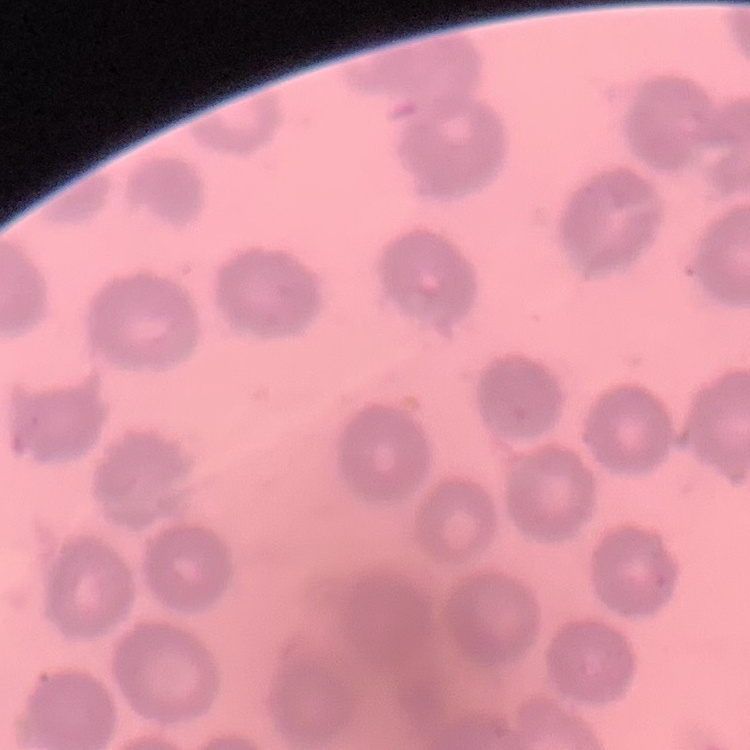
Summary:
  - Erythrocyte morphology: no rouleaux formation
  - Preparation: thin blood film
  - Image type: square crop of a larger photomicrograph
  - Stain: Field's or Giemsa